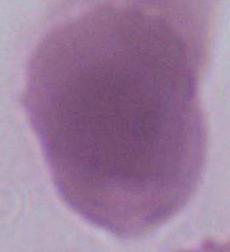

Summary:
  - Modality: micrograph
  - Magnification: 1000x
  - Identification: erythrocyte